Classify this cell by malaria status.
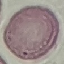

Uninfected.

Summary:
  - Image type: cell patch, automatically extracted from a larger field of view and resized to 64 × 64 pixels
  - Capture: smartphone through the microscope eyepiece
  - Preparation: thin blood film
  - Stain: Giemsa